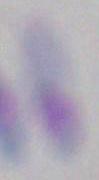
modality = micrograph
magnification = 1000x
identification = Toxoplasma gondii